Comment on the morphology of the erythrocytes.
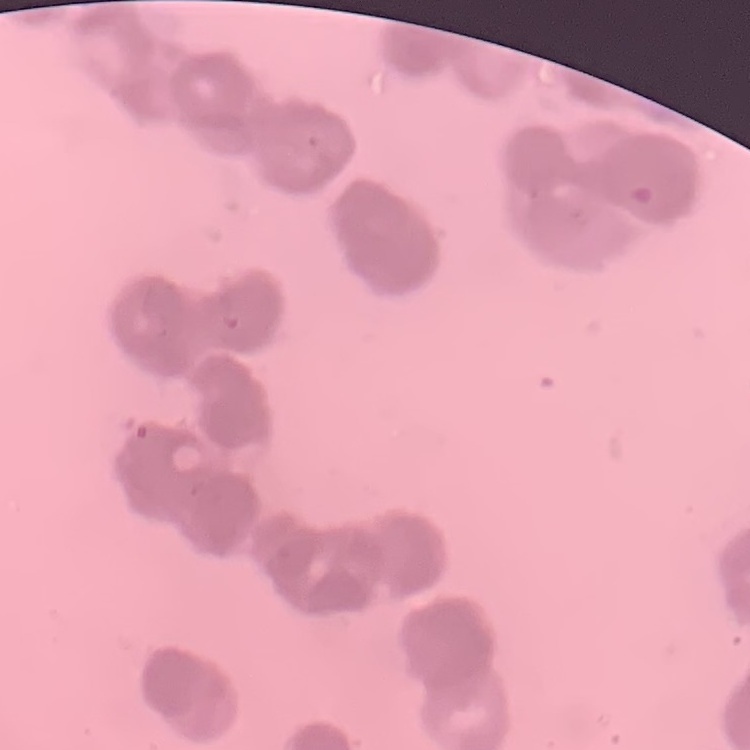

Rouleaux formation.

Thin peripheral smear. Stained with either Field's or Giemsa. One tile cut from a larger photomicrograph.